Locate white blood cells.
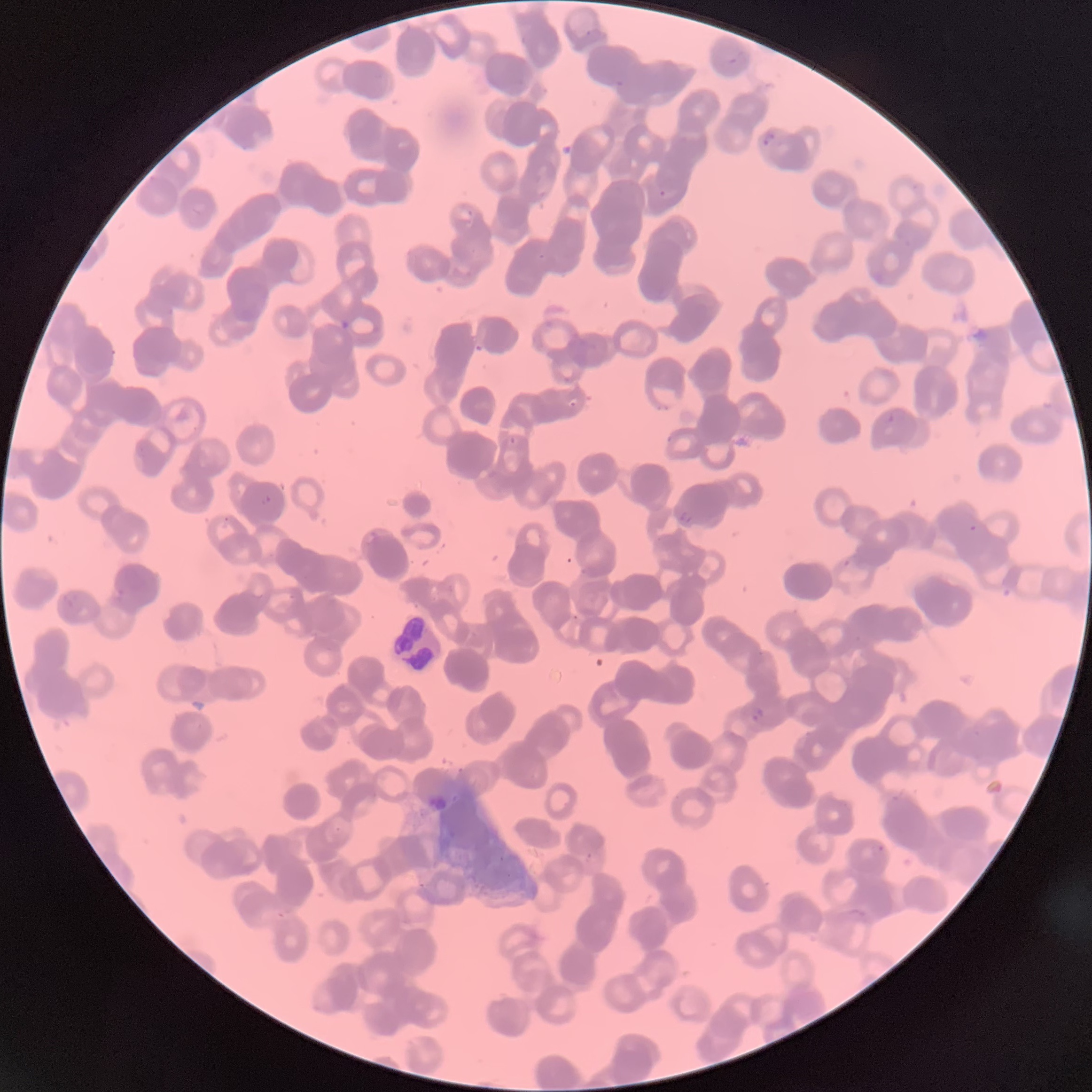

Approximate bounding boxes as (x1,y1)-(x2,y2) corner pairs in pixels.
White blood cells: (390,614)-(444,673).

Plasmodium parasite locations: (584,29)-(593,37), (762,130)-(775,147), (658,189)-(667,198), (465,206)-(474,218), (567,397)-(577,408), (877,410)-(895,429), (509,437)-(517,444), (261,495)-(271,506), (678,511)-(693,523), (968,524)-(978,535), (750,706)-(763,723), (872,842)-(885,857), (585,852)-(593,862). Thin blood film. The red blood cells show rouleaux formation. Optical microscopy. Image is 1092×1092 pixels.